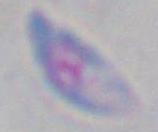

Captured at 1000x magnification. Toxoplasma gondii is seen. Photomicrograph.